Assess this cell for malaria.
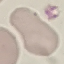
It is uninfected.

Summary:
  - Preparation: thin smear
  - Capture: smartphone through the microscope eyepiece
  - Stain: Giemsa
  - Image type: cell patch, automatically extracted from a larger field of view and resized to 64 × 64 pixels